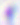

magnification: 400x
identification: Toxoplasma gondii
modality: photomicrograph